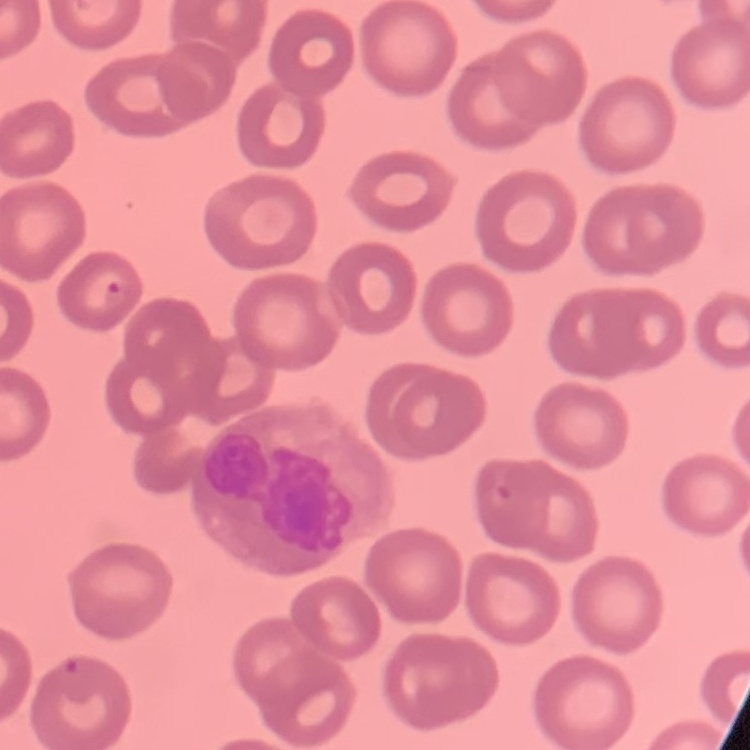 The erythrocytes exhibit no rouleaux formation. Thin blood film. One tile cut from a larger photomicrograph. Field's or Giemsa stain.